Assess the morphology of the erythrocytes.
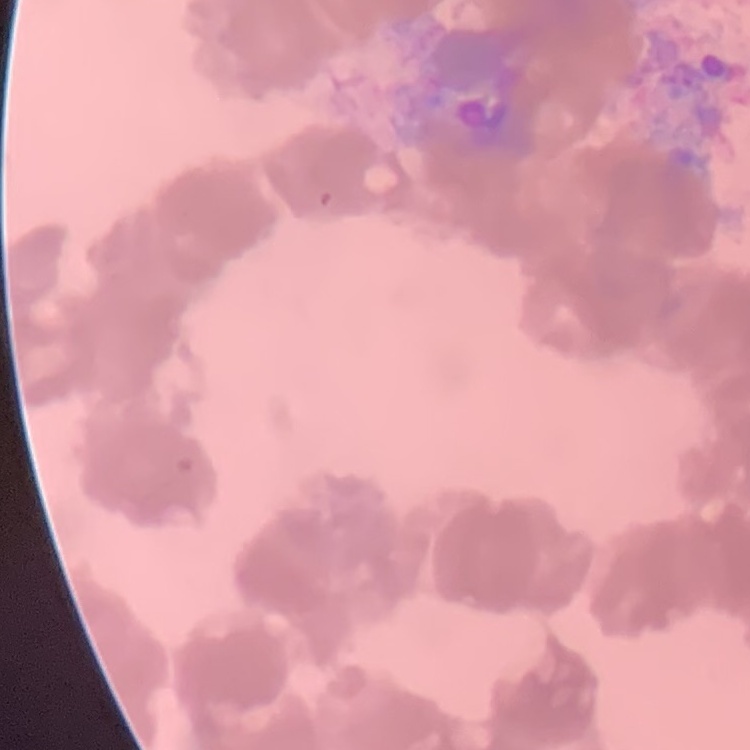

They show rouleaux formation.

Field's or Giemsa stain. One tile cut from a larger photomicrograph. Thin blood film.